Outline each blood parasite and name the species.
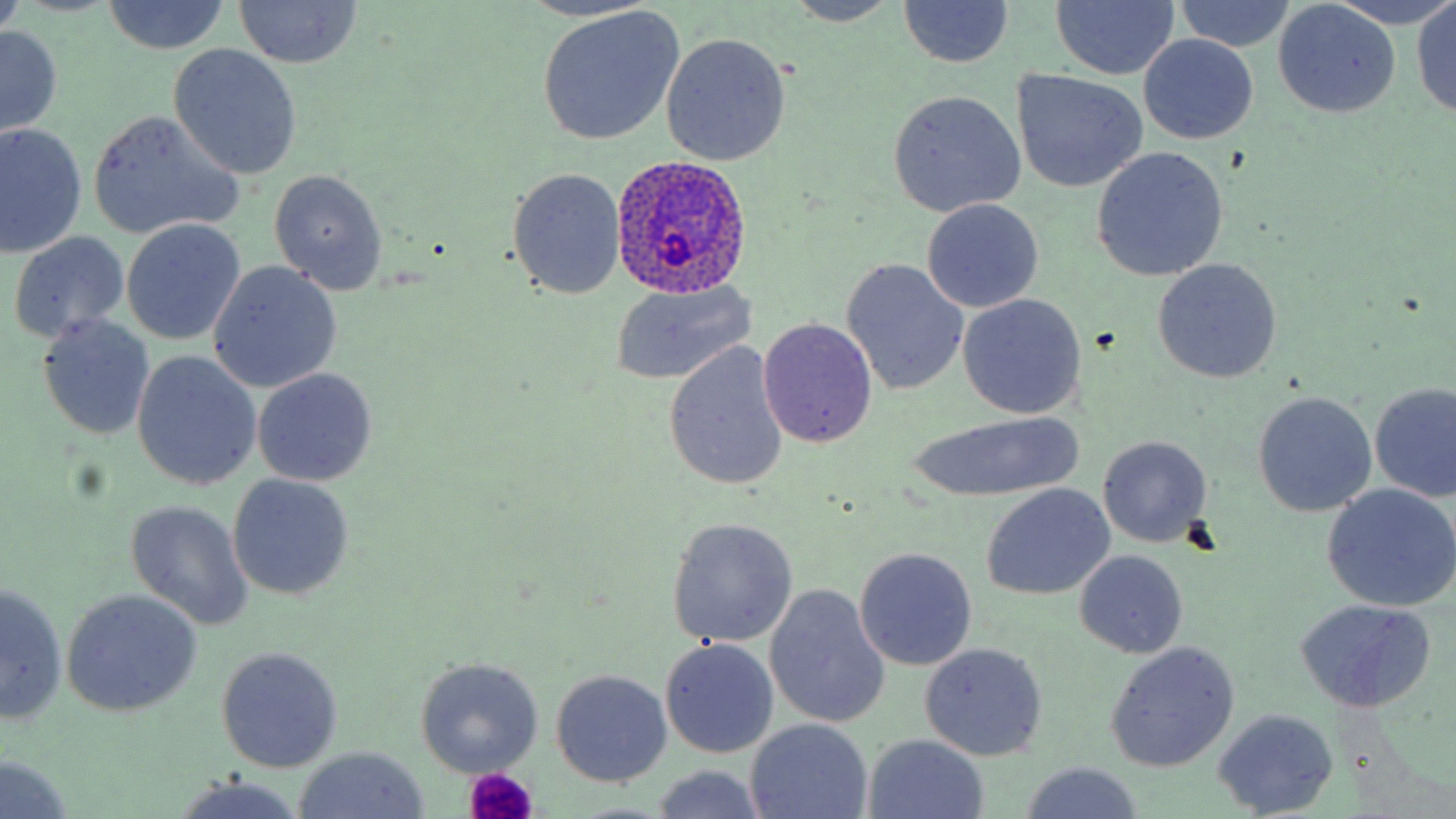

Approximate bounding boxes as (x1,y1)-(x2,y2) corner pairs in pixels.
Plasmodium ovale-infected red blood cells: (608,157)-(757,295).
No Plasmodium falciparum, Plasmodium malariae, Plasmodium vivax, Babesia divergens, or Trypanosoma brucei observed.

Summary:
  - Platelet locations: (463,768)-(541,819)
  - Uninfected red blood cell locations: (0,0)-(27,37), (895,0)-(1015,68), (1329,0)-(1456,29), (1412,0)-(1456,118), (101,1)-(231,55), (231,1)-(363,69), (783,1)-(903,26), (1051,1)-(1179,80), (1177,1)-(1294,52), (1274,2)-(1401,117), (535,6)-(686,146), (1,26)-(62,136), (661,33)-(791,165), (1139,35)-(1259,144), (169,44)-(302,180), (1015,70)-(1147,193), (886,91)-(1025,216), (88,112)-(242,239), (0,124)-(88,256), (1091,148)-(1228,281), (509,168)-(626,298), (269,170)-(389,296), (922,199)-(1043,313), (121,221)-(246,346), (8,231)-(131,347), (841,259)-(969,397), (1152,259)-(1282,383), (208,262)-(342,394), (609,283)-(756,385), (958,294)-(1086,419), (39,315)-(155,440), (760,318)-(877,449), (664,345)-(789,489), (131,351)-(262,490), (253,368)-(378,487), (1371,384)-(1456,502), (1252,391)-(1376,516), (910,411)-(1082,503), (1098,435)-(1211,548), (228,474)-(354,601), (981,484)-(1114,601), (1321,484)-(1456,612), (125,500)-(255,631), (668,517)-(797,647), (855,548)-(978,671), (1075,550)-(1187,657), (2,583)-(67,724), (766,585)-(891,728), (61,590)-(200,717), (1294,598)-(1436,714), (659,638)-(778,759), (1105,641)-(1240,772), (919,643)-(1047,760), (216,646)-(343,772), (414,657)-(544,777), (550,669)-(672,787), (1211,707)-(1337,818), (744,718)-(873,819), (863,735)-(990,818), (292,746)-(432,818), (0,753)-(76,819), (1016,761)-(1147,817), (650,765)-(768,819), (171,777)-(309,819)
  - Slide-level diagnosis: Plasmodium ovale
  - Image size: 1456×819 pixels
  - Modality: light microscopy
  - Magnification: 1000x
  - Field of view: single
  - Preparation: thin blood smear
  - Stain: May-Grünwald-Giemsa